Assess this cell for malaria.
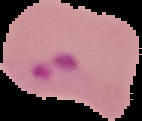
Parasitized.

image size = 142×121 pixels
preparation = thin blood smear
image type = segmented cell region on a black background